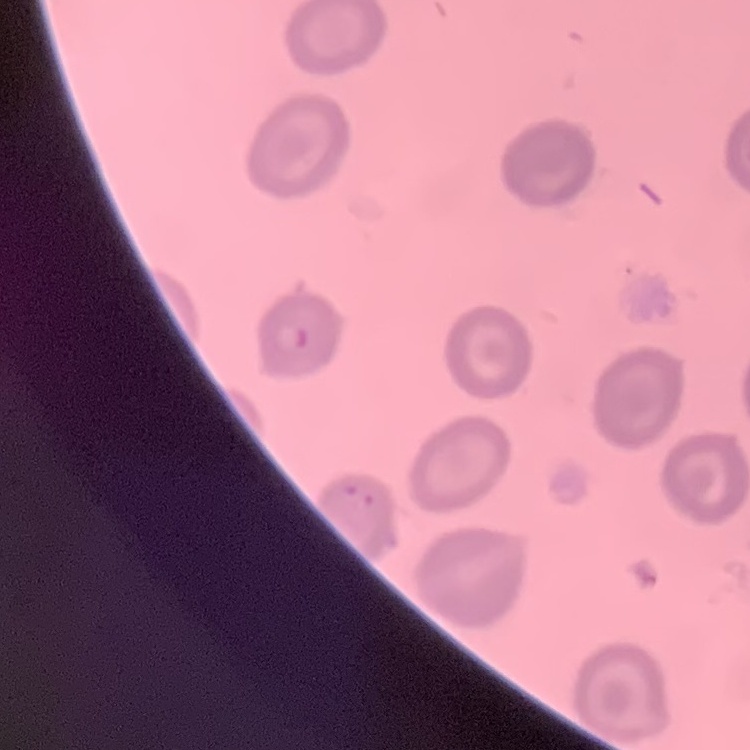 The erythrocytes show no rouleaux formation. One tile cut from a larger photomicrograph. Thin blood film. Stained with either Field's or Giemsa.